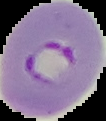

{
  "image_size": "106×121 pixels",
  "result": "malaria parasites detected",
  "preparation": "thin blood film",
  "image_type": "segmented cell region on a black background"
}